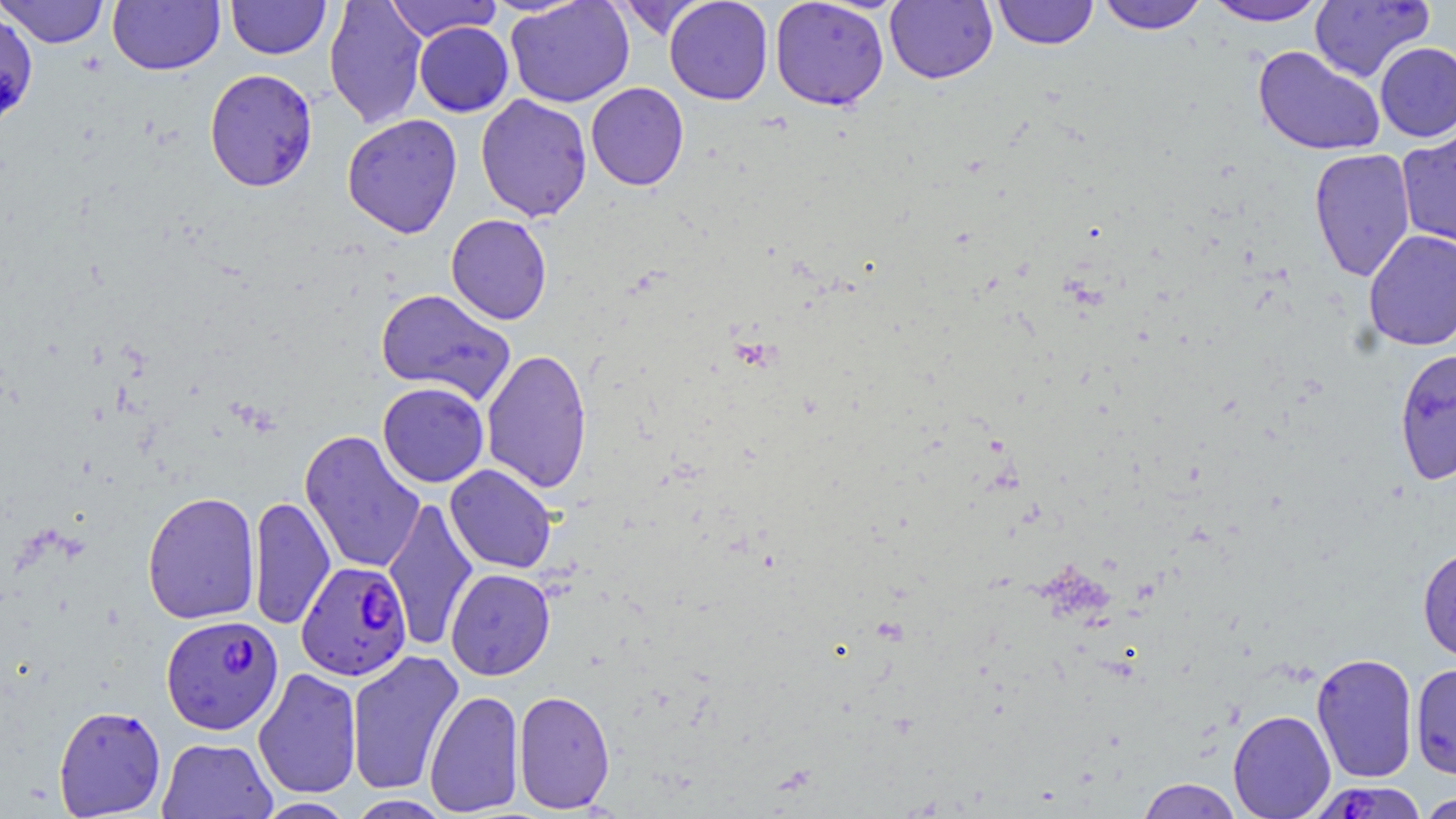

{
  "slide_level_diagnosis": "Plasmodium falciparum",
  "stain": "May-Grünwald-Giemsa",
  "modality": "optical microscopy",
  "plasmodium_falciparum_infected_red_blood_cell_locations_subset": "approximate bounding boxes as named x1/y1/x2/y2 corners in pixels: (x1=296, y1=561, x2=412, y2=680), (x1=161, y1=614, x2=284, y2=734)",
  "field_of_view": "single",
  "image_size": "1456×819 pixels",
  "uninfected_red_blood_cell_locations_subset": "approximate bounding boxes as named x1/y1/x2/y2 corners in pixels: (x1=1, y1=0, x2=110, y2=48), (x1=108, y1=0, x2=225, y2=75), (x1=226, y1=0, x2=330, y2=59), (x1=324, y1=0, x2=428, y2=129), (x1=384, y1=0, x2=501, y2=42), (x1=505, y1=0, x2=634, y2=108), (x1=613, y1=0, x2=709, y2=40), (x1=664, y1=0, x2=773, y2=105), (x1=769, y1=0, x2=890, y2=111), (x1=885, y1=0, x2=998, y2=84), (x1=992, y1=0, x2=1098, y2=49), (x1=1094, y1=0, x2=1209, y2=34), (x1=1202, y1=1, x2=1328, y2=26), (x1=1309, y1=1, x2=1434, y2=82), (x1=0, y1=8, x2=39, y2=131), (x1=414, y1=22, x2=513, y2=117), (x1=1374, y1=42, x2=1456, y2=142), (x1=1253, y1=45, x2=1386, y2=156), (x1=204, y1=68, x2=318, y2=192), (x1=586, y1=82, x2=689, y2=191), (x1=475, y1=93, x2=593, y2=222), (x1=342, y1=114, x2=463, y2=238), (x1=1397, y1=125, x2=1456, y2=250), (x1=1308, y1=148, x2=1416, y2=282), (x1=446, y1=214, x2=552, y2=324), (x1=1363, y1=230, x2=1456, y2=351), (x1=376, y1=289, x2=516, y2=403), (x1=1393, y1=347, x2=1456, y2=485), (x1=481, y1=348, x2=593, y2=494), (x1=378, y1=382, x2=489, y2=487), (x1=299, y1=429, x2=426, y2=574), (x1=444, y1=464, x2=557, y2=573), (x1=142, y1=491, x2=261, y2=625), (x1=248, y1=496, x2=335, y2=630), (x1=382, y1=497, x2=479, y2=652), (x1=1417, y1=546, x2=1456, y2=664), (x1=446, y1=568, x2=555, y2=680), (x1=346, y1=649, x2=465, y2=796), (x1=1311, y1=652, x2=1419, y2=784), (x1=1410, y1=663, x2=1456, y2=779), (x1=253, y1=667, x2=362, y2=799), (x1=513, y1=689, x2=615, y2=813), (x1=424, y1=690, x2=525, y2=815), (x1=53, y1=704, x2=166, y2=817), (x1=1227, y1=709, x2=1336, y2=819), (x1=156, y1=737, x2=277, y2=819), (x1=1136, y1=778, x2=1243, y2=819), (x1=1416, y1=791, x2=1456, y2=819), (x1=345, y1=795, x2=452, y2=818), (x1=252, y1=797, x2=358, y2=818)",
  "magnification": "1000x",
  "preparation": "thin blood smear"
}